Locate every blood parasite and identify its species.
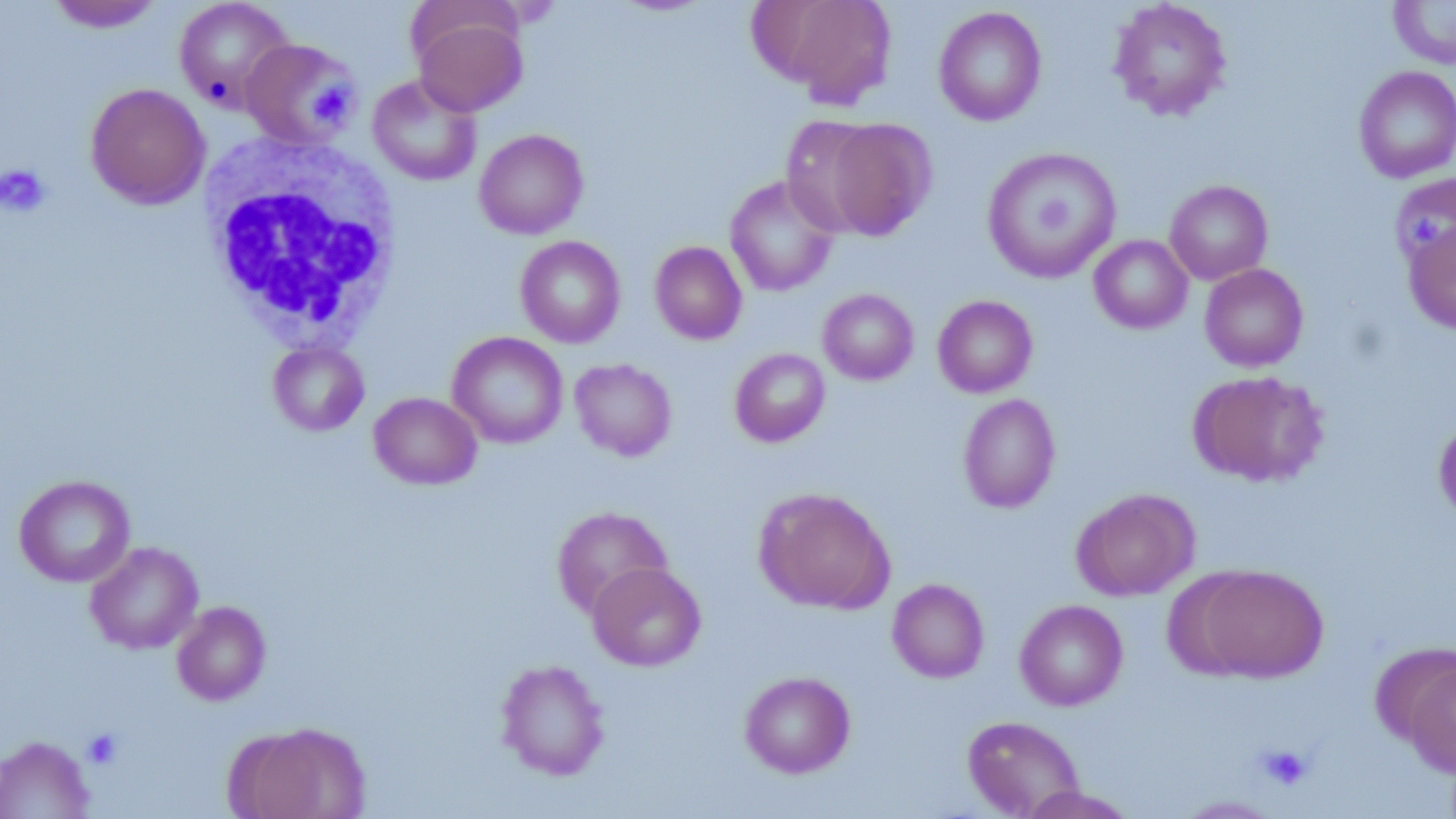

No blood parasites observed.

Approximate bounding boxes as (x1, y1, x2, y2) in pixels. Platelet locations (subset): (311, 83, 351, 123), (0, 164, 50, 217), (1409, 214, 1444, 253), (81, 729, 123, 769), (1257, 744, 1312, 790). Uninfected red blood cell locations (subset): (45, 0, 165, 33), (173, 0, 295, 112), (754, 0, 899, 109), (1108, 0, 1232, 121), (1388, 0, 1456, 69), (933, 6, 1047, 127), (412, 13, 528, 118), (1353, 65, 1456, 183), (367, 74, 482, 186), (85, 83, 210, 209), (780, 115, 886, 235), (821, 117, 937, 240), (474, 129, 588, 239), (982, 146, 1122, 284), (1389, 173, 1456, 271), (724, 174, 840, 297), (1164, 180, 1273, 285), (1404, 219, 1456, 335), (1089, 234, 1193, 334), (515, 235, 626, 348), (650, 241, 747, 345), (1200, 263, 1309, 372), (818, 288, 919, 385), (933, 295, 1038, 398), (447, 331, 568, 449), (268, 340, 369, 435), (730, 348, 830, 447), (570, 358, 676, 461), (1188, 370, 1328, 487), (369, 392, 482, 490), (958, 393, 1060, 513), (1434, 415, 1456, 524), (14, 474, 135, 587), (754, 486, 895, 614), (1071, 487, 1199, 600), (552, 505, 673, 618), (85, 541, 203, 654), (588, 562, 706, 671), (1196, 565, 1328, 682), (887, 578, 990, 683), (1015, 599, 1128, 711), (172, 601, 271, 705), (1371, 643, 1455, 747), (496, 659, 610, 780), (1404, 662, 1455, 777), (739, 671, 855, 778), (963, 715, 1085, 818), (238, 722, 373, 819), (0, 735, 94, 818), (1018, 785, 1138, 819), (1174, 795, 1284, 818). White blood cell locations: (200, 133, 404, 346). Slide-level diagnosis: negative for blood parasites. Image is 1456×819 pixels. Light microscopy. May-Grünwald-Giemsa stain. One field of a larger specimen. 1000x magnification. Thin blood smear.